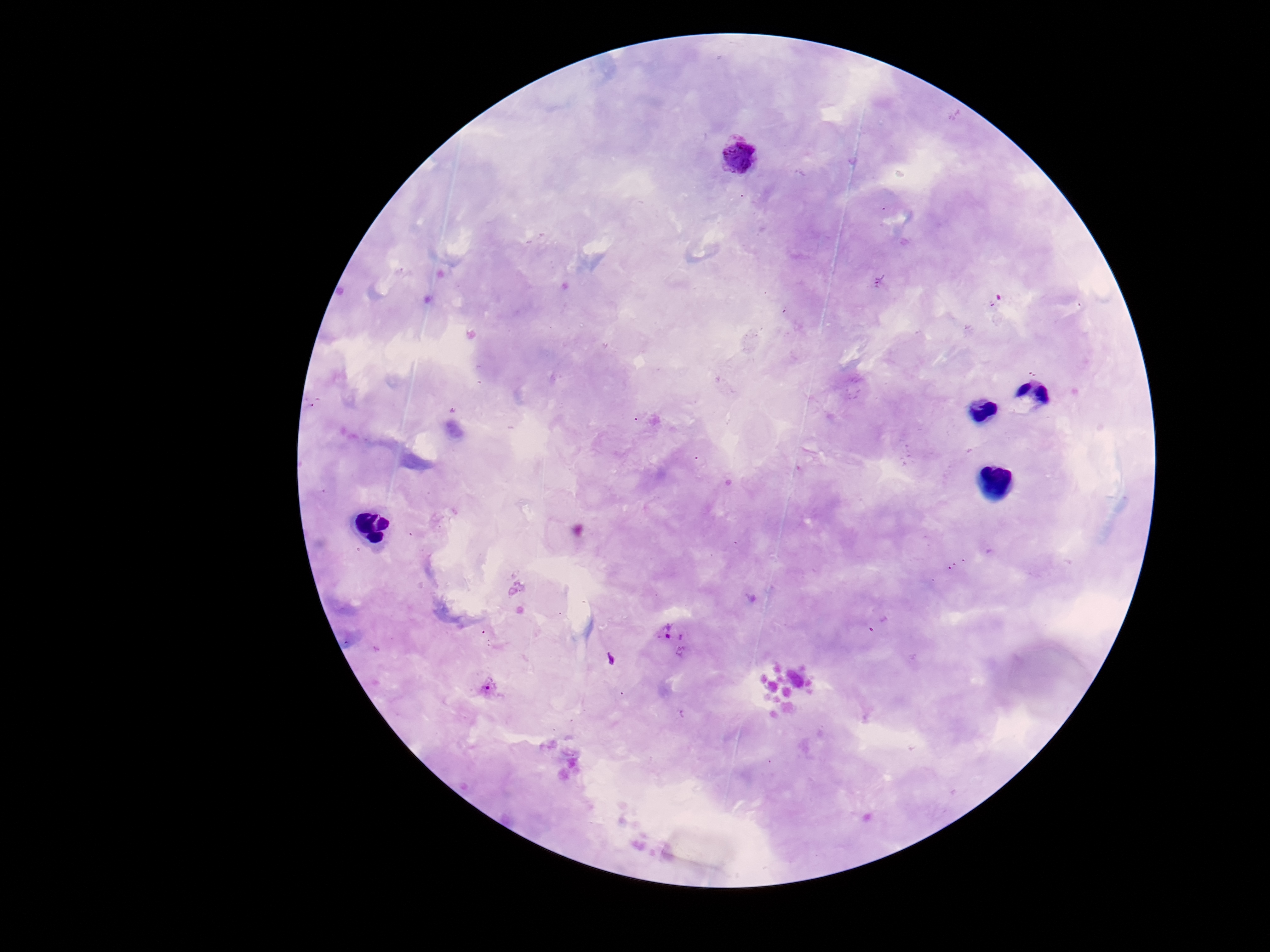

Approximate centers as {x, y} in pixels.
Summary:
  - Plasmodium parasite locations: {739, 156}, {673, 635}, {488, 689}
  - Field of view: single
  - Capture: smartphone camera through the microscope eyepiece
  - Stain: Giemsa
  - Magnification: 100x
  - Patient malaria status: positive
  - Preparation: thick peripheral-blood smear
  - Image size: 1270×952 pixels